Assess the background quality.
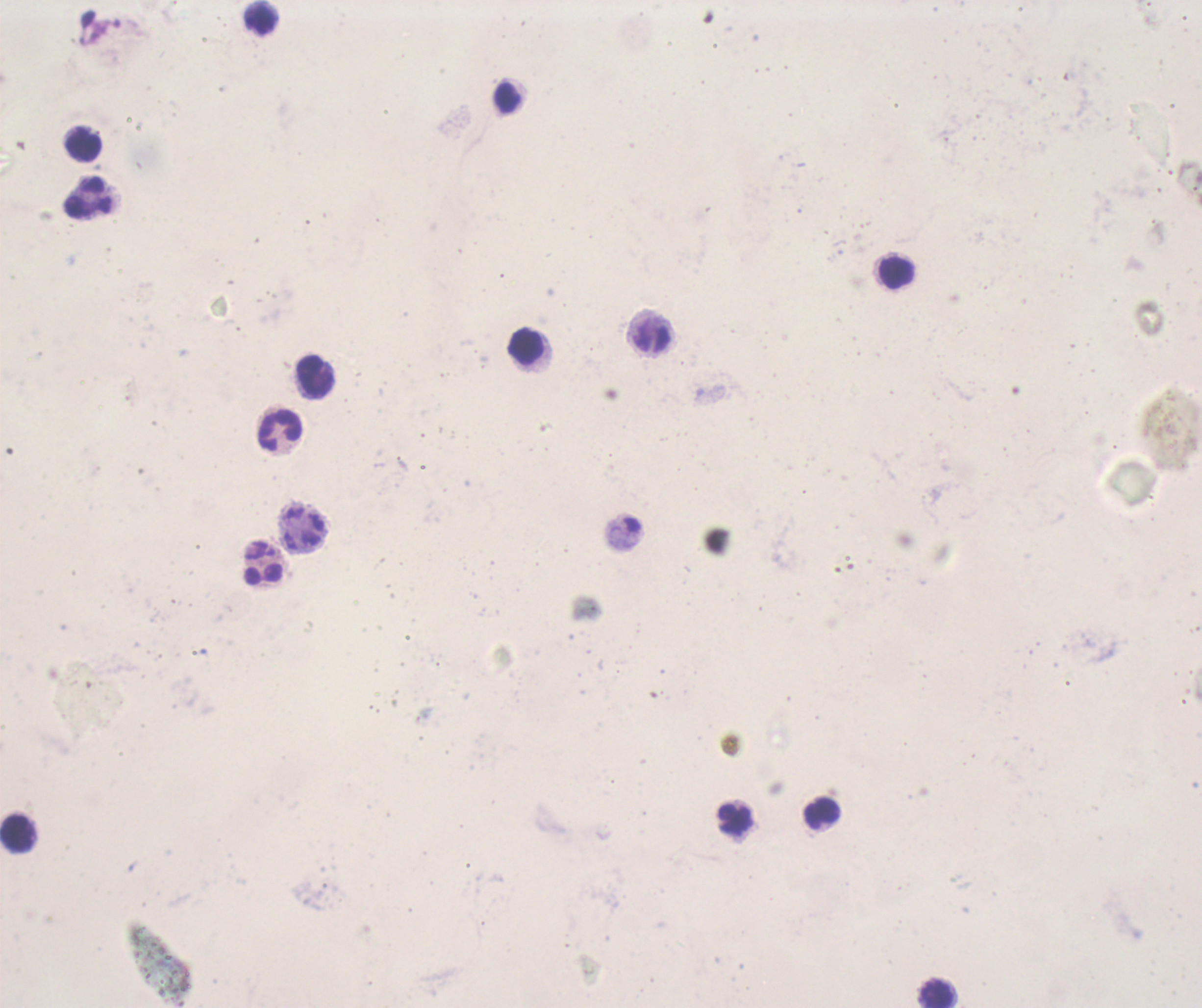

It is poor.

Approximate object centers, in pixels from the top-left corner.
Summary:
  - Leukocyte locations: (x=263, y=18), (x=506, y=98), (x=85, y=145), (x=86, y=197), (x=895, y=271), (x=526, y=346), (x=314, y=376), (x=281, y=430), (x=263, y=574), (x=821, y=814), (x=733, y=819), (x=20, y=834), (x=936, y=992)
  - Field of view: one from this slide
  - Coloration quality: bad
  - Preparation: thick blood film
  - Magnification: 100x
  - Image size: 1202×1008 pixels
  - Result: no malaria parasites seen
  - Context: previously used in a real diagnosis
  - Stain: Romanowsky